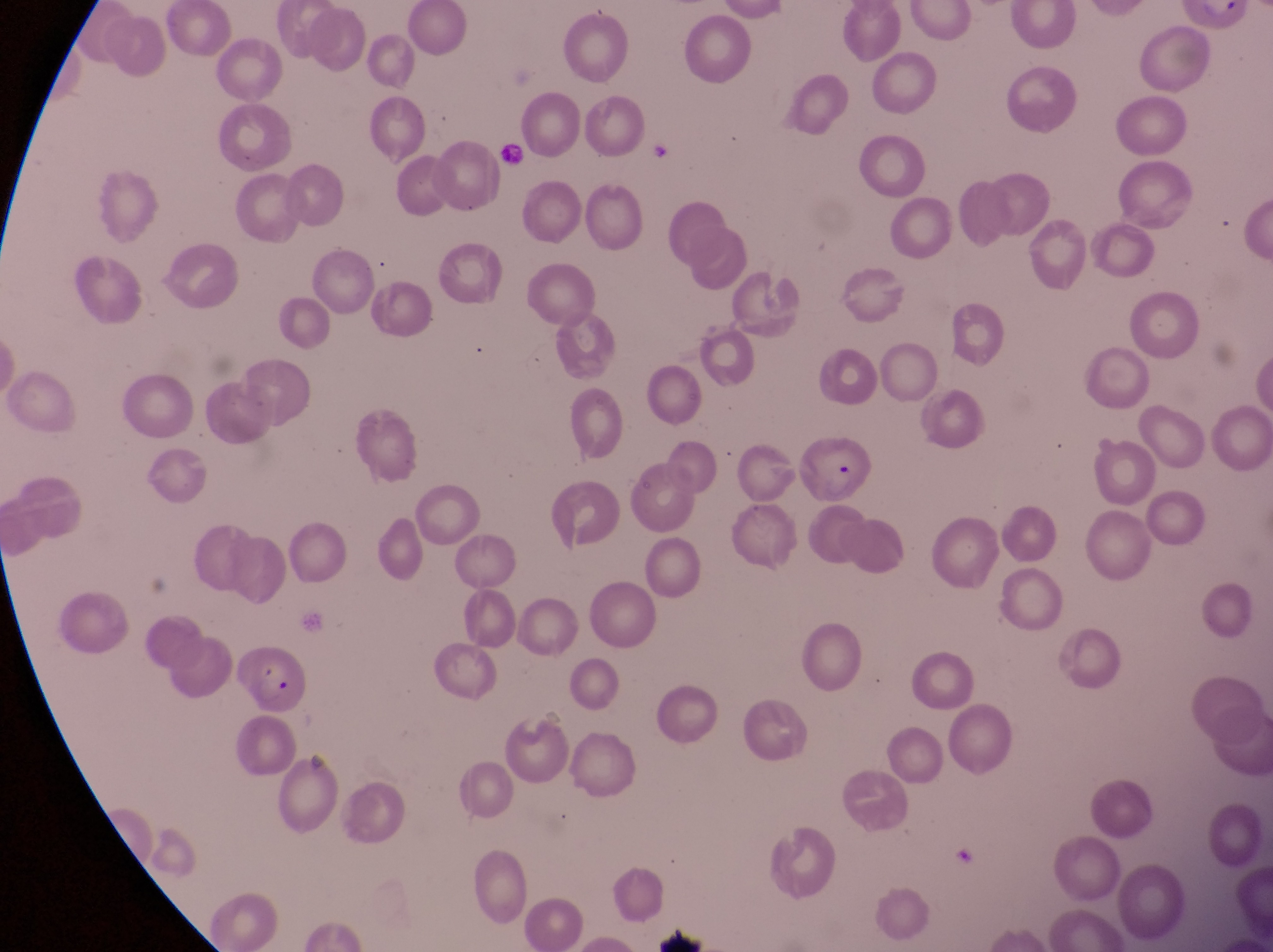
Approximate bounding boxes as {left, top, right, bottom} in pixels. Artifact (platelet-like body, stain precipitate, or debris) locations: {646, 128, 681, 170}. Parasitised red blood cell locations: {794, 437, 877, 509}, {230, 644, 313, 718}. Photographed through the eyepiece of an Olympus CX-23 microscope with a smartphone camera. Single field of view. Image is 1273×952 pixels. At a magnification of 1000x. Sample from Uganda. Thin blood film.